Outline each blood parasite and name the species.
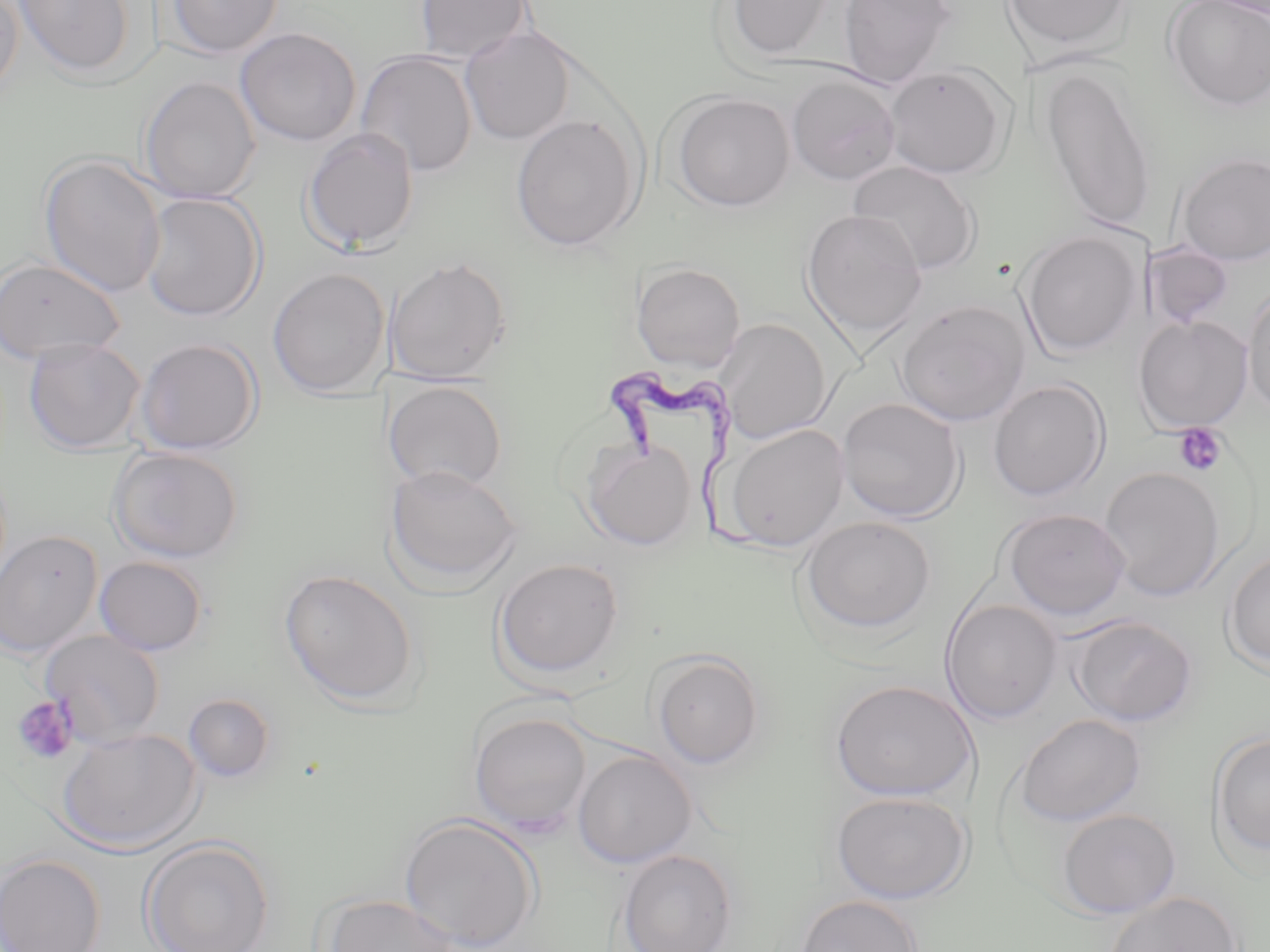

Approximate bounding boxes as [x1, y1, x2, y2] in pixels.
Trypanosoma brucei: [606, 370, 764, 559].
No Plasmodium falciparum, Plasmodium ovale, Plasmodium malariae, Plasmodium vivax, or Babesia divergens observed.

slide_level_diagnosis: Trypanosoma brucei
image_size: 1270×952 pixels
modality: light microscopy
magnification: 1000x
platelet_locations_subset: 'approximate bounding boxes as [x1, y1, x2, y2] in pixels: [1173, 423, 1228, 477], [12, 695, 80, 766]'
stain: May-Grünwald-Giemsa
uninfected_red_blood_cell_locations_subset: 'approximate bounding boxes as [x1, y1, x2, y2] in pixels: [0, 0, 24, 103], [13, 0, 136, 79], [165, 0, 283, 58], [413, 0, 534, 63], [723, 0, 837, 61], [838, 0, 957, 89], [1001, 0, 1134, 54], [1164, 0, 1270, 112], [459, 26, 576, 145], [235, 27, 361, 147], [355, 50, 478, 177], [884, 64, 1011, 179], [1039, 66, 1158, 235], [785, 74, 902, 185], [139, 76, 261, 204], [670, 92, 795, 211], [510, 113, 642, 252], [300, 127, 420, 255], [1176, 152, 1270, 266], [38, 153, 167, 298], [847, 161, 982, 277], [139, 192, 266, 322], [801, 209, 928, 343], [1017, 230, 1145, 357], [1144, 243, 1234, 331], [385, 256, 512, 385], [0, 257, 125, 365], [630, 262, 746, 372], [268, 268, 390, 398], [1243, 287, 1270, 416], [895, 298, 1031, 426], [1133, 316, 1254, 433], [715, 317, 832, 444], [135, 336, 262, 455], [23, 337, 145, 453], [987, 379, 1110, 501], [383, 380, 508, 494], [836, 397, 967, 523], [724, 423, 850, 552], [583, 437, 697, 551], [107, 446, 244, 562], [383, 463, 524, 593], [1099, 466, 1225, 601], [999, 508, 1132, 621], [799, 515, 937, 636], [0, 530, 103, 658], [1222, 550, 1270, 675], [93, 556, 209, 656], [492, 557, 624, 680], [280, 569, 420, 708], [940, 599, 1063, 724], [1067, 614, 1197, 727], [649, 649, 765, 770], [830, 678, 978, 802], [183, 693, 275, 782], [468, 710, 592, 834], [1013, 713, 1147, 827], [57, 727, 203, 854], [1210, 731, 1270, 859], [572, 750, 697, 868], [829, 789, 973, 905], [1056, 808, 1182, 919], [399, 813, 542, 951], [139, 837, 274, 952], [616, 849, 738, 952], [0, 853, 106, 952], [1104, 891, 1242, 952], [319, 893, 462, 951], [794, 894, 923, 952]'
preparation: thin blood film
field_of_view: single